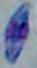 Toxoplasma gondii is shown. Micrograph. Captured at 1000x magnification.